Give the position of every Plasmodium parasite visible.
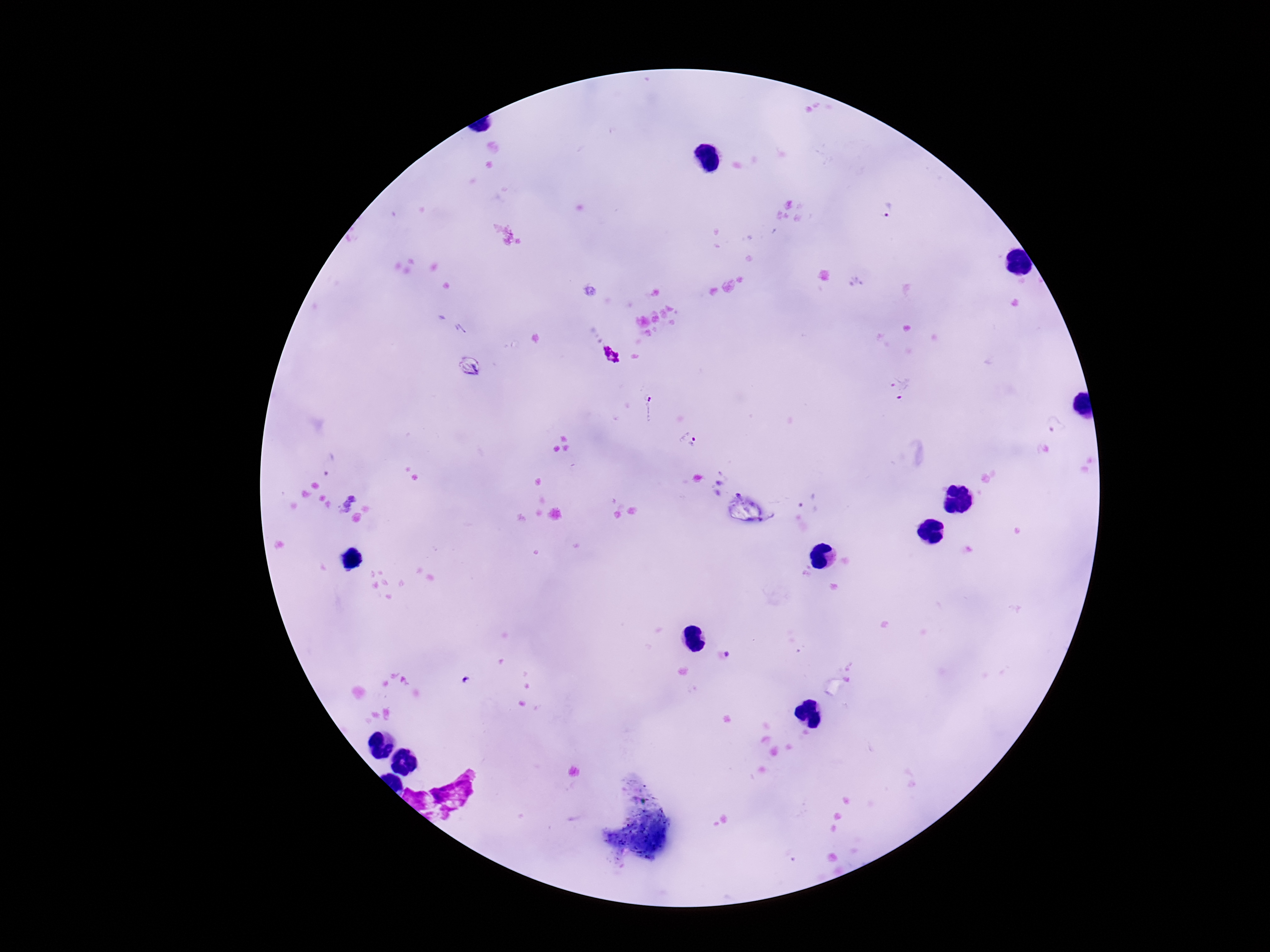

Approximate centers as (x, y) in pixels.
Plasmodium parasites: (887, 212), (902, 388), (648, 409), (1056, 428), (688, 440), (327, 464), (347, 503), (809, 503), (726, 657).

Giemsa-stained preparation. Thick peripheral-blood smear. 100x magnification. Smartphone photograph taken through the microscope eyepiece. Patient malaria status: positive. Single field of view. Image is 1270×952 pixels.